Describe the morphology of the red blood cells.
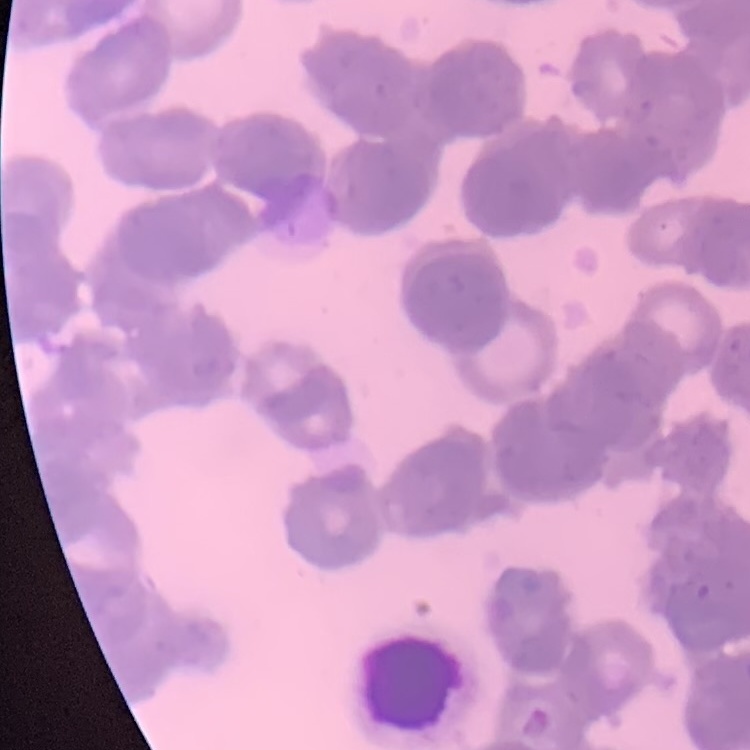

Rouleaux formation.

preparation = thin blood film
stain = Field's or Giemsa
image type = square crop of a larger photomicrograph